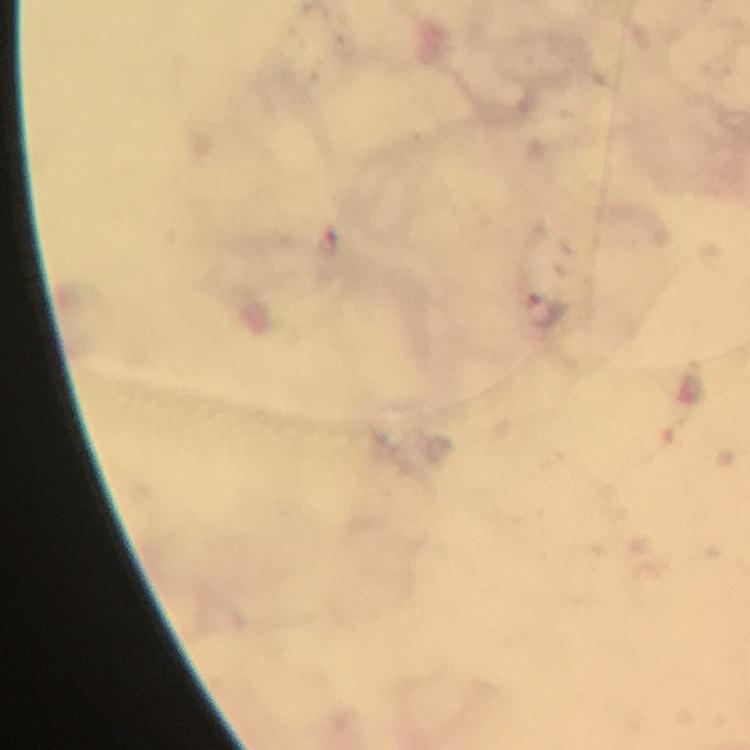 Approximate centers as {x, y} in pixels. Plasmodium parasite locations: {545, 311}. Giemsa stain. Image is 750×750 pixels. Thick smear. A crop from one field of view. At 100x magnification. Immersion oil was used. From a diagnostic examination for malaria. Photographed through the microscope with a smartphone camera.